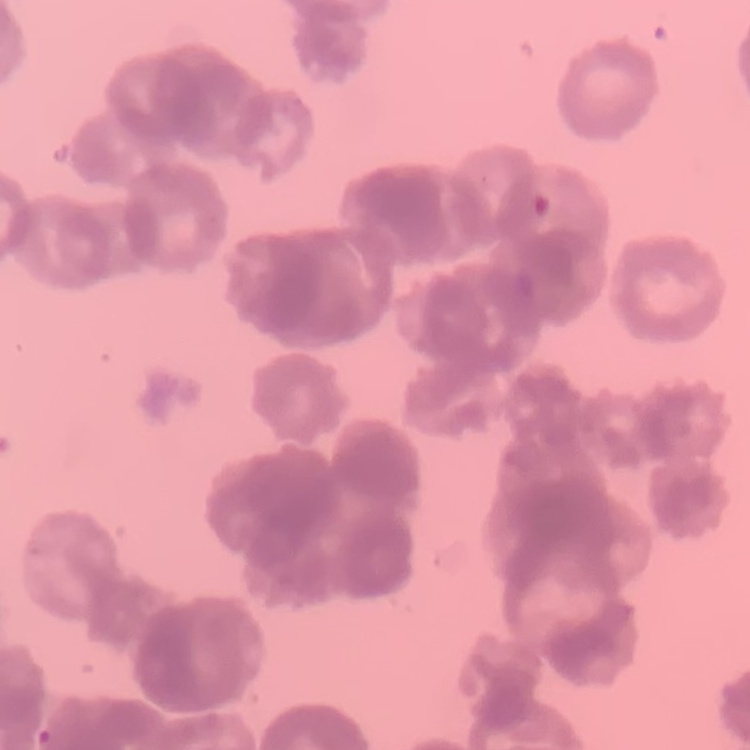
The red blood cells exhibit rouleaux formation. Stained with either Field's or Giemsa. Square crop of a larger photomicrograph. Thin blood smear.